Identify the blood parasite species.
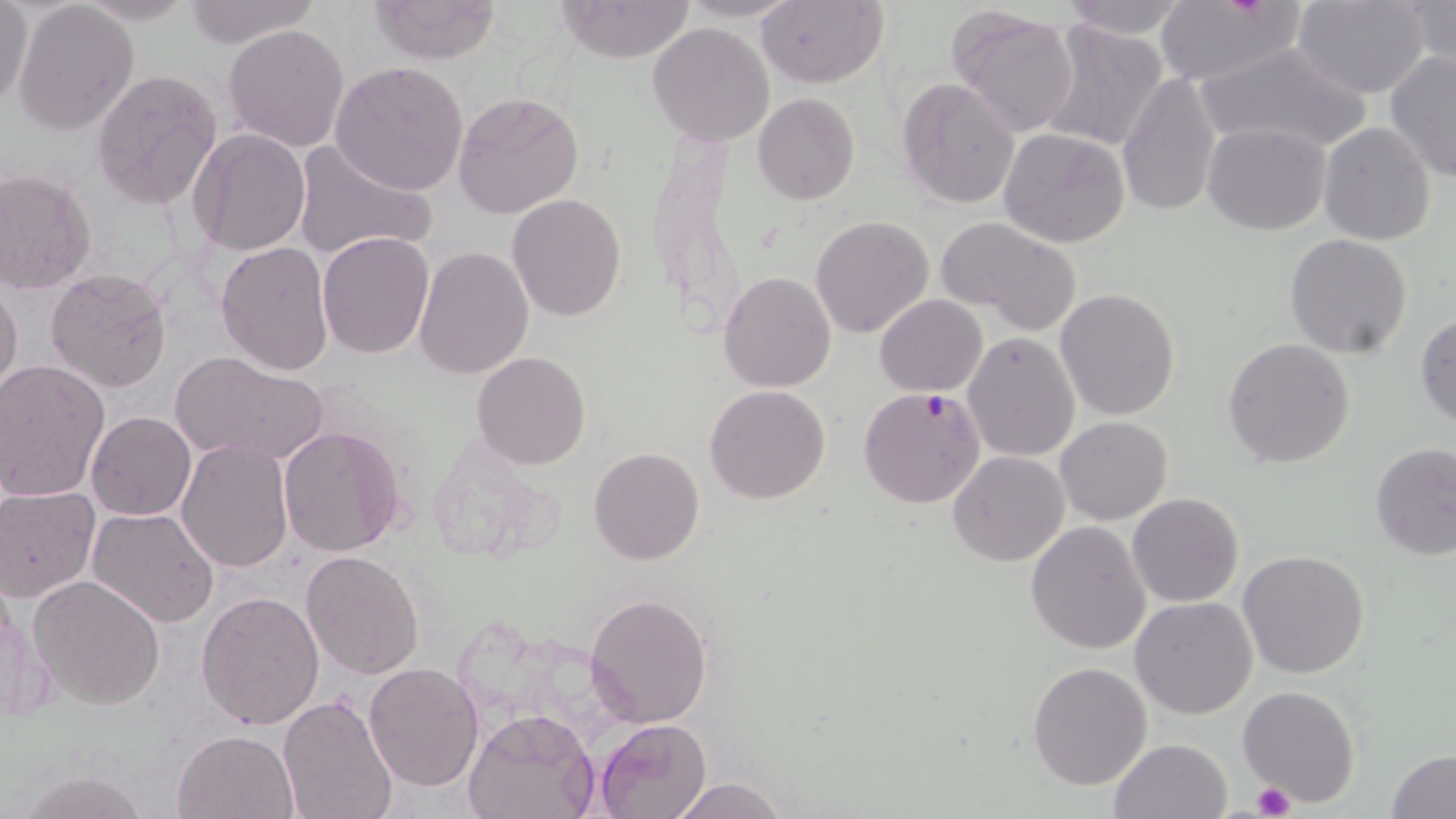
Plasmodium falciparum.

Approximate bounding boxes as (x1,y1)-(x2,y2) corner pairs in pixels. Platelet locations: (1251,782)-(1295,818). Uninfected red blood cell locations: (1,0)-(32,108), (368,0)-(502,64), (557,0)-(696,64), (678,0)-(803,22), (1057,0)-(1190,40), (180,1)-(318,49), (756,1)-(886,88), (1296,1)-(1432,99), (1404,1)-(1455,75), (13,2)-(140,136), (1153,2)-(1302,88), (947,7)-(1081,138), (1039,20)-(1170,153), (648,22)-(774,145), (223,24)-(348,153), (1191,42)-(1372,157), (1384,50)-(1456,181), (330,61)-(471,195), (92,69)-(222,211), (1118,71)-(1223,220), (897,76)-(1020,208), (452,90)-(586,219), (754,93)-(860,205), (1202,121)-(1333,236), (1304,123)-(1424,358), (1318,123)-(1436,245), (998,125)-(1131,247), (187,128)-(312,257), (292,137)-(437,259), (0,169)-(96,293), (508,194)-(628,321), (810,215)-(933,339), (939,215)-(1082,332), (316,231)-(434,359), (1284,233)-(1413,359), (216,240)-(337,376), (413,244)-(532,380), (45,267)-(172,393), (719,272)-(836,391), (0,280)-(23,401), (1056,289)-(1181,421), (875,294)-(987,396), (1415,313)-(1456,428), (964,331)-(1080,463), (1223,337)-(1355,468), (170,350)-(329,468), (471,351)-(591,469), (0,360)-(109,501), (705,384)-(830,504), (86,411)-(196,521), (1055,416)-(1173,526), (277,424)-(408,558), (176,438)-(293,574), (418,439)-(557,563), (1370,444)-(1456,561), (589,447)-(705,565), (948,450)-(1069,566), (0,485)-(99,603), (1127,494)-(1245,607), (87,507)-(220,628), (1026,520)-(1151,655), (1238,550)-(1370,678), (300,551)-(424,680), (30,574)-(166,710), (196,589)-(325,728), (586,591)-(714,728), (1130,596)-(1258,718), (1027,661)-(1152,791), (364,662)-(484,791), (1238,685)-(1360,807), (278,695)-(398,819), (462,706)-(599,819), (594,718)-(711,819), (174,729)-(298,818), (1107,738)-(1235,819), (1385,748)-(1456,819), (16,771)-(152,818), (669,777)-(792,819). Plasmodium falciparum-infected red blood cell locations: (855,384)-(985,512). One field of a larger specimen. Optical microscopy. 1000x magnification. May-Grünwald-Giemsa stain. Thin blood film. Image is 1456×819 pixels.